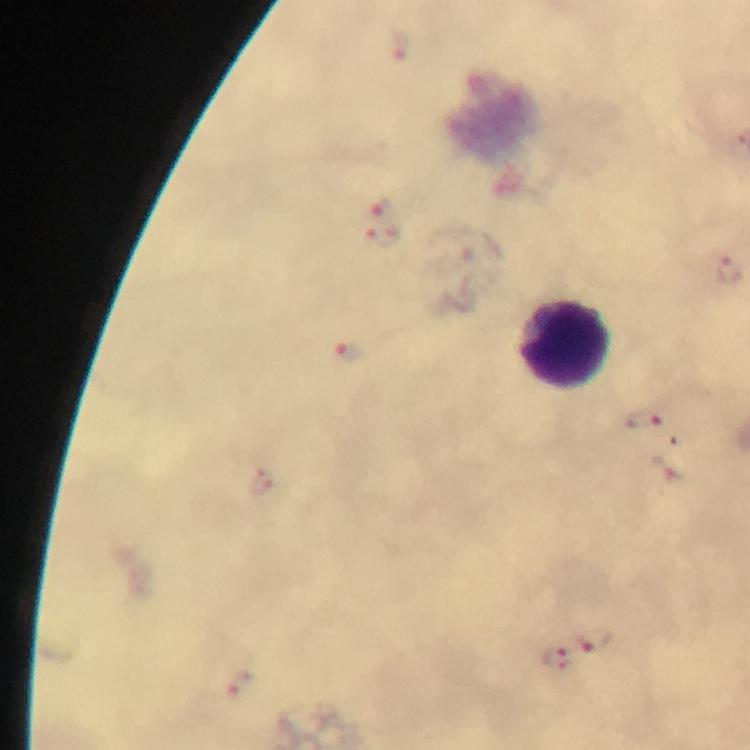
{
  "magnification": "100x",
  "context": "from a malaria diagnostic workup",
  "image_size": "750×750 pixels",
  "capture": "smartphone mounted on the microscope",
  "immersion_oil": "used",
  "preparation": "thick blood film",
  "malaria_parasite_locations": "approximate centers as {x, y} in pixels: {402, 48}, {382, 207}, {382, 237}, {729, 268}, {345, 352}, {646, 424}, {260, 484}, {595, 638}, {557, 656}, {241, 684}",
  "stain": "Giemsa",
  "leukocyte_locations": "approximate centers as {x, y} in pixels: {566, 345}",
  "cropped_from": "one field of view"
}